Mark where leukocytes are.
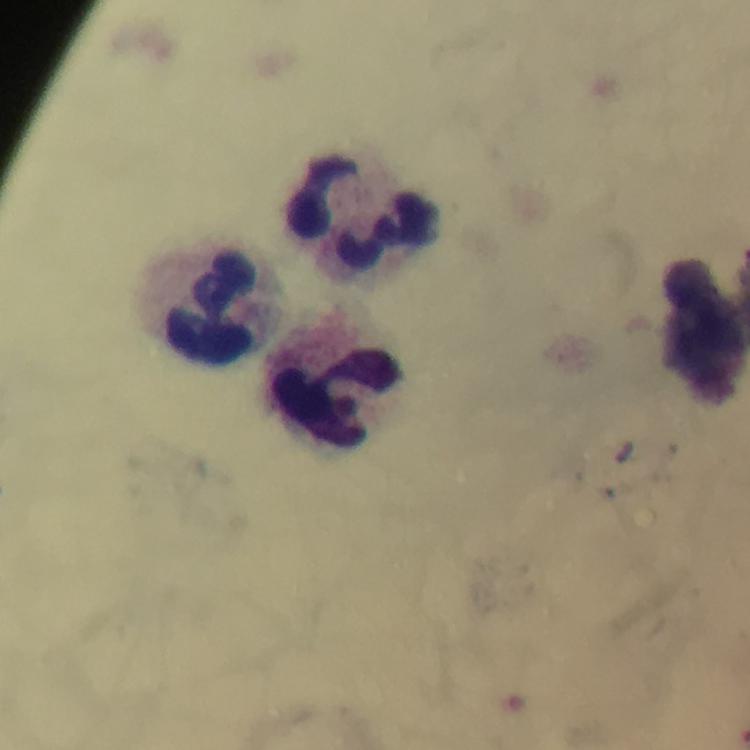
Approximate centers as (x, y) in pixels.
Leukocytes: (367, 212), (211, 304), (339, 399).

malaria parasites = none detected
capture = smartphone mounted on the microscope
image size = 750×750 pixels
stain = Giemsa
context = from a malaria diagnostic workup
cropped from = a single field of view
preparation = thick smear
magnification = 100x
immersion oil = used